Evaluate for malaria.
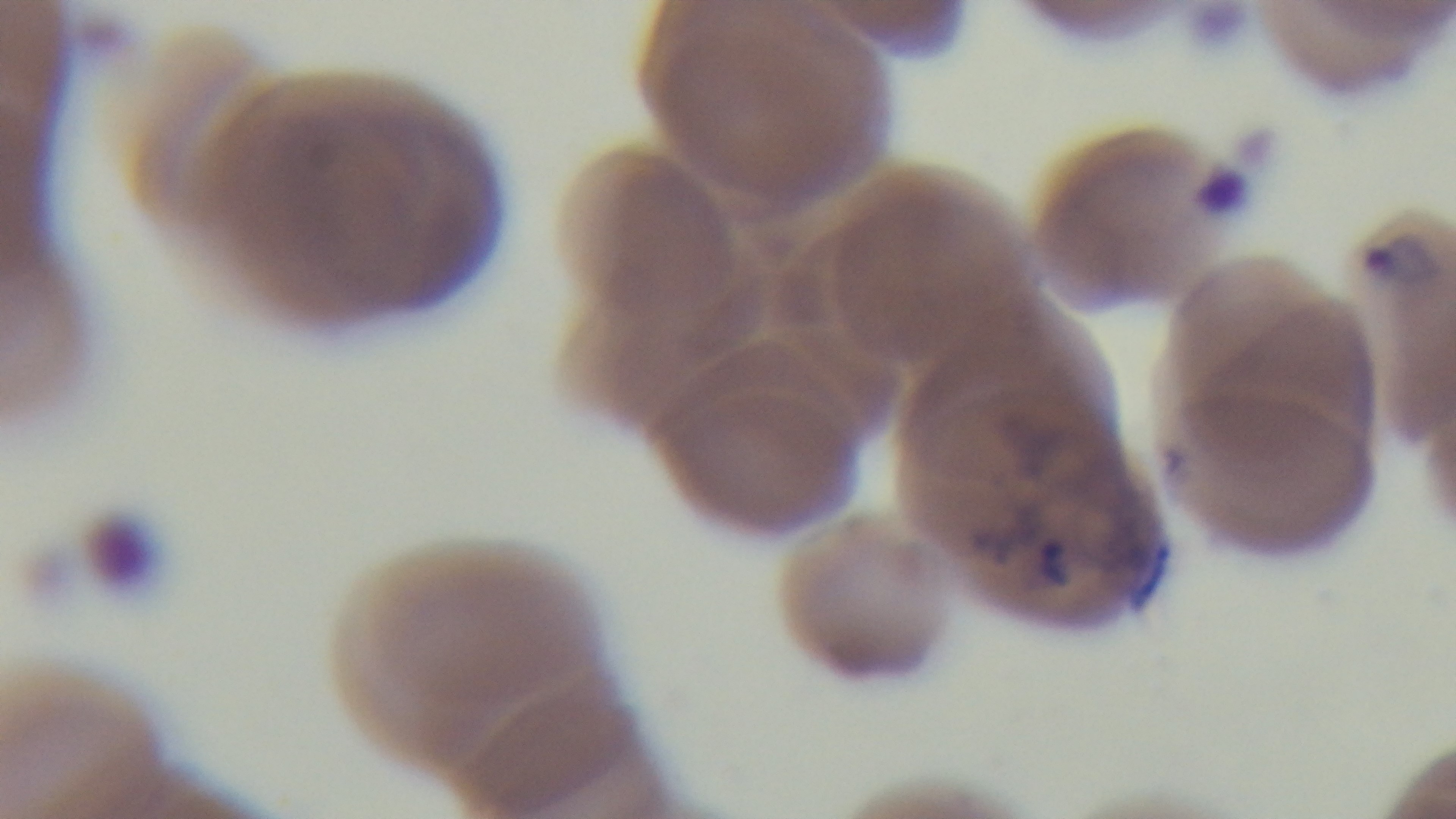
It is infected.

Single field of view. Giemsa-stained. Mounted 4K digital camera. Photomicrograph. Preparation: thin blood film. Oil-immersion objective, 100x.